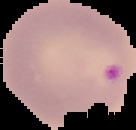

Summary:
  - Preparation: thin blood film
  - Image type: segmented cell region on a black background
  - Image size: 136×130 pixels
  - Malaria status: parasitized